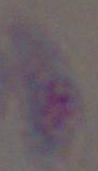
1000x magnification. Toxoplasma gondii is shown. Photomicrograph.